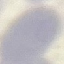
Summary:
  - Malaria status: uninfected
  - Capture: smartphone through the microscope eyepiece
  - Preparation: thin smear
  - Image type: cell patch, automatically extracted from a larger field of view and resized to 64 × 64 pixels
  - Stain: Giemsa